Report the malaria status of this cell.
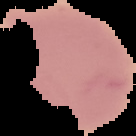

It is uninfected.

Summary:
  - Preparation: thin blood smear
  - Image size: 136×136 pixels
  - Image type: cell region segmented out of the field of view; surrounding area masked to black